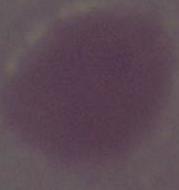

{
  "magnification": "1000x",
  "identification": "erythrocyte",
  "modality": "photomicrograph"
}